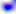
Summary:
  - Magnification: 400x
  - Modality: micrograph
  - Identification: Toxoplasma gondii